Classify this cell by malaria status.
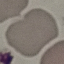
Uninfected.

image type = automatically extracted cell patch, resized to 64 × 64 pixels
stain = Giemsa
capture = smartphone through the microscope eyepiece
preparation = thin blood film